Identify the blood parasite species.
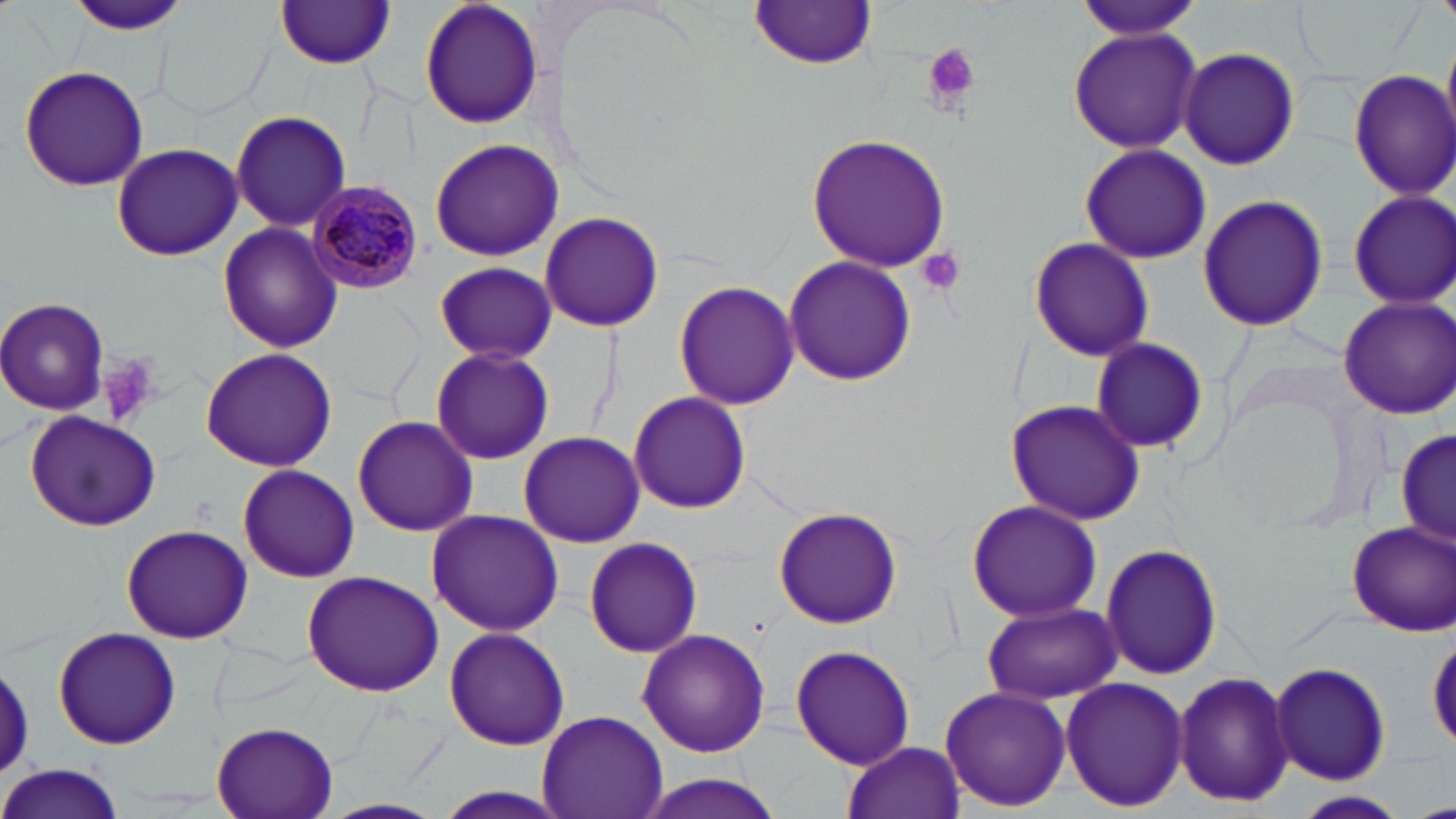
Plasmodium malariae.

preparation: thin blood smear
plasmodium_malariae_infected_red_blood_cell_locations: 'approximate bounding boxes as (x1, y1, x2, y2) in pixels: (308, 182, 425, 295)'
modality: optical microscopy
platelet_locations: 'approximate bounding boxes as (x1, y1, x2, y2) in pixels: (923, 43, 981, 105), (917, 246, 965, 294), (100, 353, 163, 425)'
image_size: 1456×819 pixels
stain: May-Grünwald-Giemsa
uninfected_red_blood_cell_locations: 'approximate bounding boxes as (x1, y1, x2, y2) in pixels: (418, 0, 546, 130), (1076, 0, 1202, 41), (65, 1, 194, 36), (274, 2, 399, 69), (748, 2, 880, 70), (156, 5, 271, 122), (1066, 24, 1204, 154), (1178, 47, 1299, 171), (18, 63, 150, 193), (1349, 66, 1456, 201), (230, 109, 352, 231), (806, 131, 952, 272), (429, 139, 564, 262), (111, 141, 243, 260), (1078, 141, 1211, 265), (1345, 190, 1455, 309), (1196, 193, 1330, 334), (540, 211, 664, 330), (218, 223, 339, 354), (1027, 236, 1155, 361), (784, 255, 917, 387), (435, 261, 557, 360), (674, 282, 799, 409), (1336, 295, 1456, 420), (0, 298, 110, 415), (1089, 337, 1211, 456), (430, 347, 554, 465), (199, 349, 337, 471), (629, 392, 750, 511), (1005, 398, 1146, 526), (26, 410, 161, 528), (352, 414, 478, 537), (1394, 427, 1455, 548), (518, 431, 646, 548), (235, 464, 361, 584), (964, 499, 1101, 623), (774, 506, 903, 630), (426, 508, 563, 637), (1346, 519, 1455, 634), (120, 524, 254, 644), (584, 537, 701, 657), (1098, 544, 1227, 683), (301, 571, 444, 697), (977, 602, 1122, 703), (51, 627, 182, 751), (444, 627, 570, 750), (637, 628, 771, 757), (790, 644, 916, 769), (0, 658, 33, 782), (1271, 660, 1392, 788), (1173, 670, 1295, 808), (1059, 678, 1188, 812), (939, 685, 1071, 813), (536, 708, 669, 819), (211, 719, 341, 819), (843, 739, 965, 819), (1, 764, 125, 819), (630, 774, 794, 817), (1290, 791, 1409, 818)'
magnification: 1000x
field_of_view: one of a larger specimen